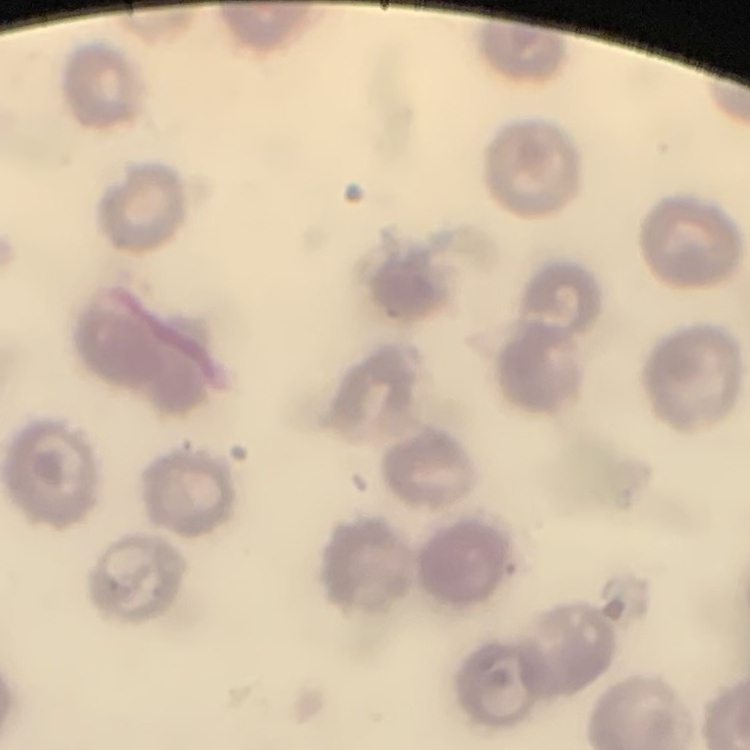 The red blood cells exhibit no rouleaux formation. Field's or Giemsa stain. Thin peripheral smear. Square crop of a larger photomicrograph.